Assess this cell for malaria.
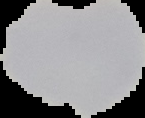
Parasitized.

Summary:
  - Image type: segmented cell region on a black background
  - Image size: 145×118 pixels
  - Preparation: thin blood film